Classify this cell by malaria status.
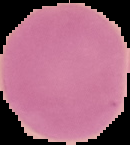

It is uninfected.

image type = cell region segmented out of the field of view; surrounding area masked to black
image size = 130×145 pixels
preparation = thin blood film